Point out each Plasmodium parasite.
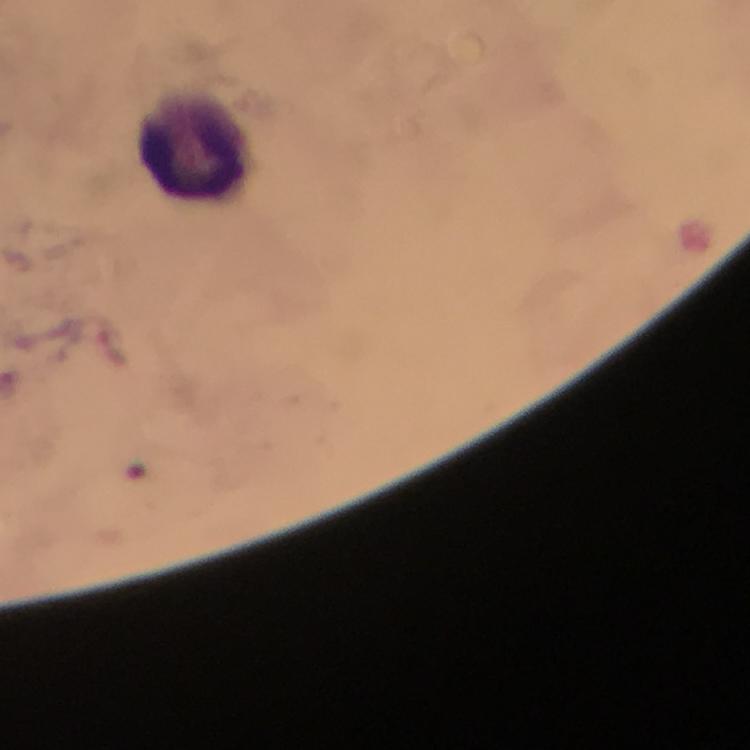

No Plasmodium parasites detected.

stain = Giemsa
image size = 750×750 pixels
capture = smartphone mounted on the microscope
immersion oil = used
leukocyte locations = approximate centers as [x, y] in pixels: [195, 147]
cropped from = a single field of view
magnification = 100x
preparation = thick blood smear
context = from a malaria diagnostic workup